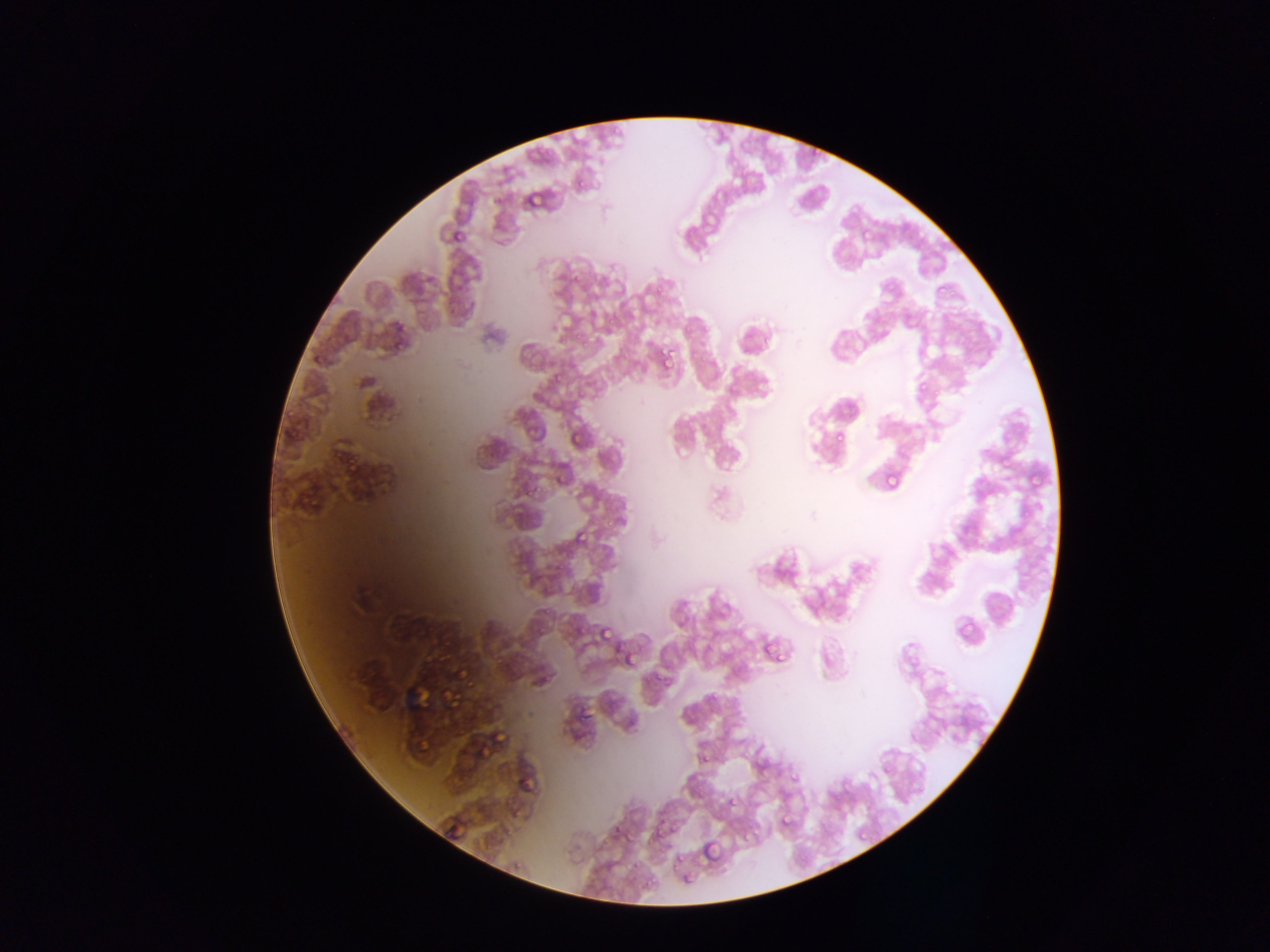 Approximate bounding boxes as left top right bottom in pixels. Plasmodium parasite locations: 805 148 824 162; 570 176 589 189; 525 190 542 208; 453 221 470 239; 572 271 585 283; 652 281 664 291; 935 285 944 294; 903 312 912 321; 608 313 620 329; 572 326 582 337; 394 339 406 350; 578 343 589 354; 656 352 674 369; 313 357 325 371; 526 357 543 369; 555 375 564 386; 917 379 930 393; 574 390 587 402; 282 412 299 429; 385 417 400 425; 833 430 845 443; 567 432 582 446; 996 449 1019 469; 343 452 361 472; 998 453 1012 466; 1028 467 1043 490; 884 471 901 488; 559 473 569 487; 524 479 534 497; 532 481 546 493; 305 496 322 512; 606 518 617 530; 572 529 588 547; 544 602 556 622; 956 618 975 639; 573 620 587 639; 598 626 612 641; 534 633 544 645; 438 638 452 653; 760 640 776 658; 765 640 786 661; 623 648 637 664; 490 653 511 668; 465 665 479 686; 651 668 667 682; 537 669 554 694; 442 689 462 708; 712 692 720 701; 494 725 513 746; 698 753 710 764; 790 774 800 784; 699 783 707 795; 728 798 741 809; 778 814 792 828; 610 817 624 836; 672 823 681 830; 623 825 642 844; 650 829 658 841; 855 829 866 840; 700 840 719 861; 676 852 685 863; 679 866 695 887. Single field of view. Photographed through a microscope with a mobile-phone camera. Image is 1270×952 pixels. Sample from Ghana. Thin blood smear.